Assess the morphology of the erythrocytes.
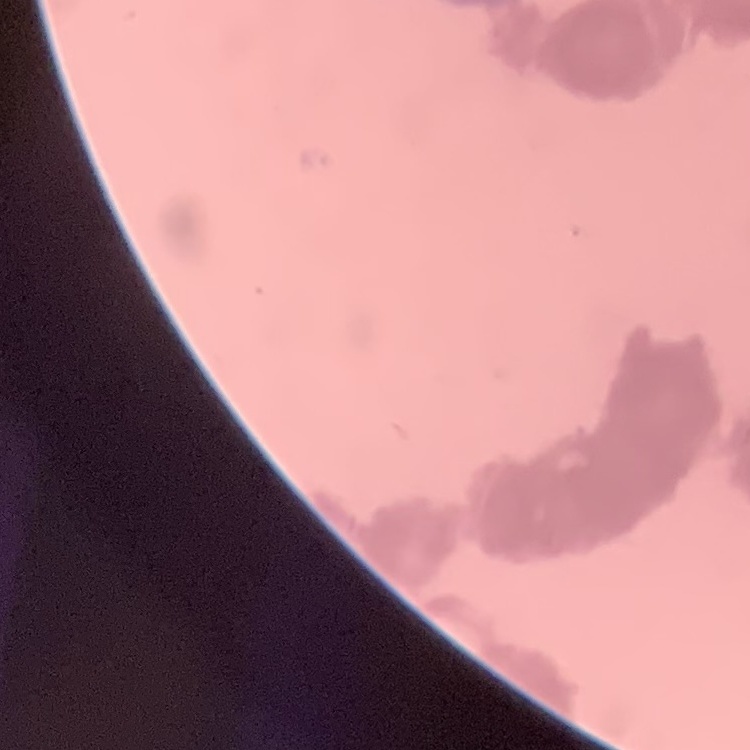

Rouleaux formation.

Square crop of a larger photomicrograph. Thin blood film. Field's or Giemsa stain.